Assess this cell for malaria.
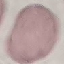
It is uninfected.

Photographed with a smartphone camera at the microscope eyepiece. Giemsa-stained preparation. Automatically extracted cell patch, resized to 64 × 64 pixels. Thin blood film.